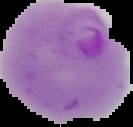
image size = 133×127 pixels
result = Plasmodium parasites identified
preparation = thin blood smear
image type = segmented cell region with the area outside set to black